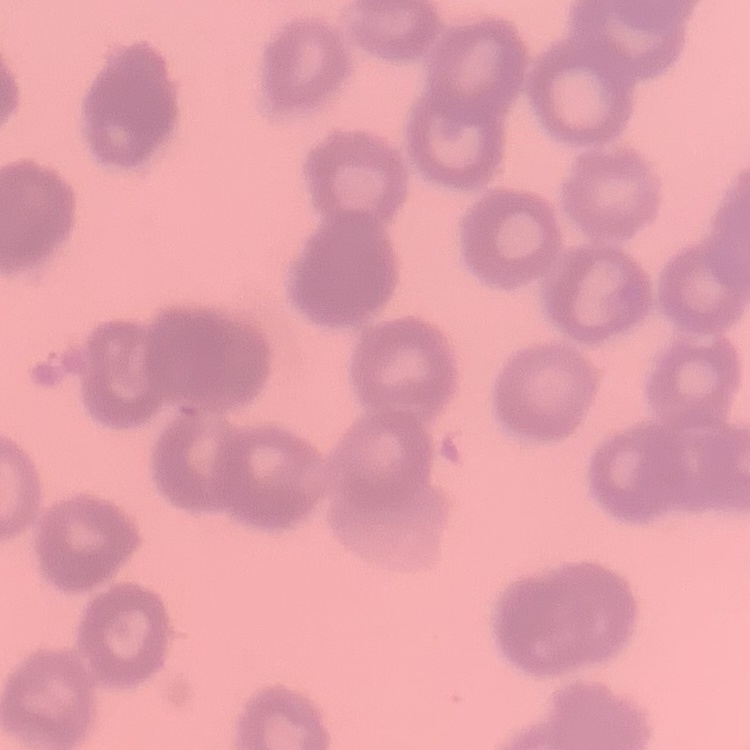
The red blood cells show rouleaux formation. Thin blood film. Stained with either Field's or Giemsa. Square crop of a larger photomicrograph.